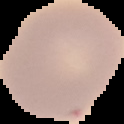

Malaria status: uninfected. Image is 124×124 pixels. From a thin blood film. The area outside the segmented cell region is set to black.